Give the position of every leukocyte visible.
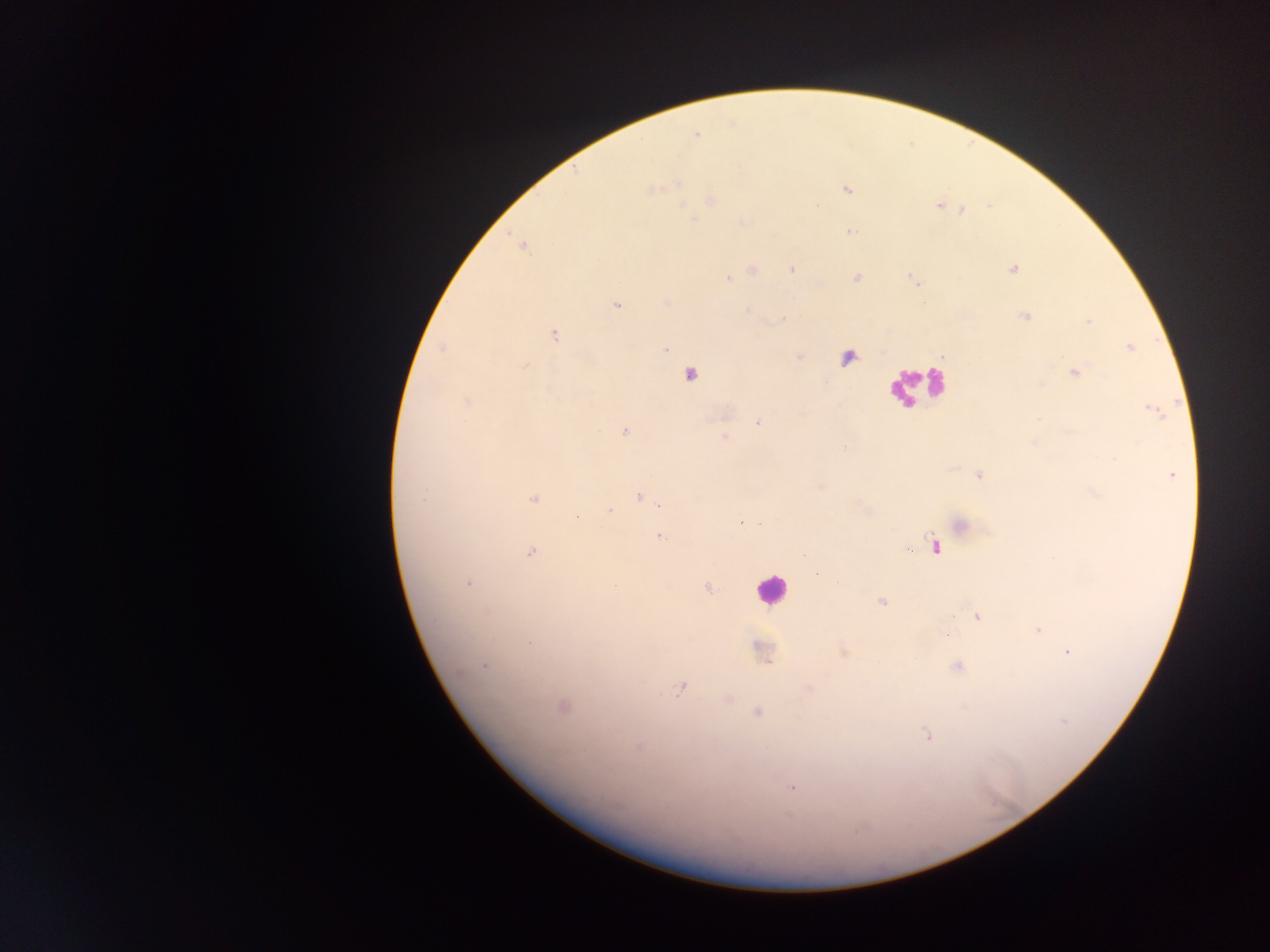

Approximate centers as x y in pixels.
Leukocytes: 768 593.

Plasmodium parasite locations: 653 190; 846 190; 680 201; 939 205; 963 210; 694 217; 849 231; 1012 268; 791 269; 750 271; 856 277; 727 278; 616 305; 749 309; 1024 315; 780 320; 1088 323; 553 335; 1130 347; 665 350; 799 356; 524 366; 1074 372; 690 374; 465 402; 1155 410; 757 421; 624 432; 724 436; 978 474; 1171 474; 821 486; 1093 492; 639 496; 533 499; 660 504; 868 510; 608 511; 740 519; 749 521; 961 525; 759 526; 659 535; 932 544; 530 550; 468 582; 614 584; 707 587; 881 600; 976 616; 1037 630; 946 635; 1067 652; 842 653; 485 665; 955 667; 680 687; 808 690; 727 700; 561 707; 964 709; 756 712; 1063 722; 927 735; 639 748; 790 788. Sample from Ghana. One field of view. Image is 1270×952 pixels. Photographed through a microscope with a mobile-phone camera. Thick blood film.